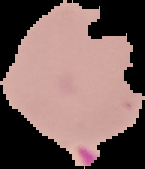
Result: no Plasmodium parasites seen. From a thin blood smear. Image is 145×169 pixels. Segmented cell region on a black background.